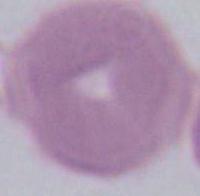

An erythrocyte is shown. Captured at 1000x magnification. Photomicrograph.